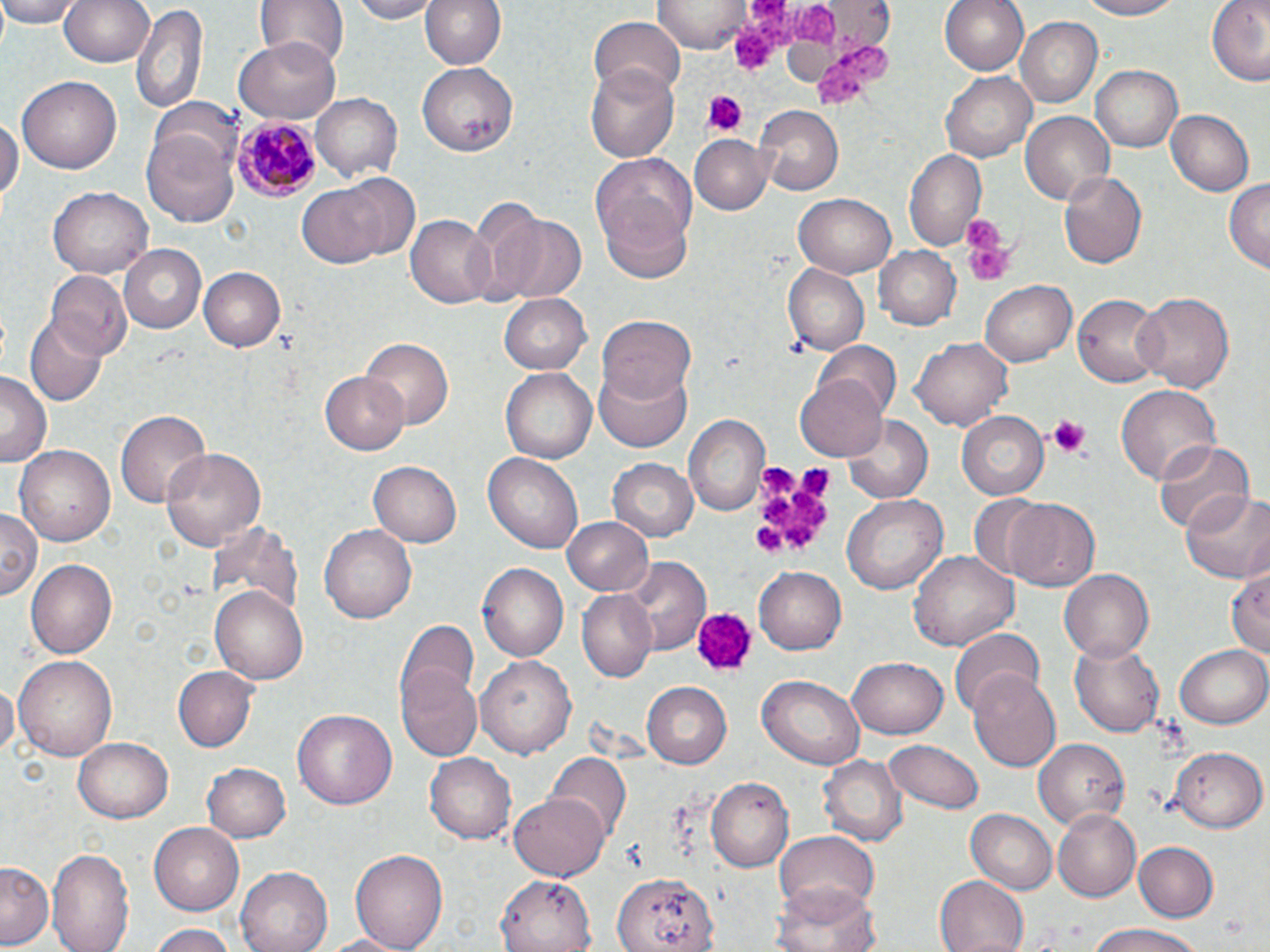

Summary:
  - Coordinate format: approximate bounding boxes as (x1, y1, x2, y2) in pixels
  - Uninfected red blood cell locations: (0, 0, 84, 27), (59, 0, 151, 68), (258, 0, 346, 68), (346, 0, 439, 22), (418, 0, 510, 70), (940, 0, 1031, 77), (1078, 0, 1189, 21), (1208, 0, 1270, 85), (652, 1, 755, 53), (131, 2, 208, 115), (590, 16, 686, 96), (1015, 17, 1101, 107), (234, 38, 342, 122), (417, 63, 519, 154), (1089, 65, 1183, 152), (585, 66, 679, 161), (941, 72, 1035, 162), (18, 76, 121, 174), (311, 94, 402, 181), (150, 98, 243, 175), (755, 107, 842, 196), (1166, 109, 1255, 196), (1021, 110, 1115, 204), (0, 113, 21, 205), (142, 130, 241, 228), (691, 133, 773, 212), (903, 147, 988, 254), (592, 152, 697, 271), (1058, 168, 1147, 271), (296, 174, 414, 270), (1224, 180, 1270, 273), (48, 187, 152, 279), (794, 194, 897, 277), (489, 212, 584, 301), (406, 215, 497, 307), (876, 245, 962, 331), (118, 246, 207, 333), (784, 260, 873, 354), (200, 266, 285, 352), (45, 271, 132, 360), (980, 279, 1077, 367), (1133, 291, 1232, 394), (498, 292, 591, 373), (1074, 292, 1165, 388), (27, 316, 106, 402), (597, 317, 695, 408), (358, 336, 454, 432), (913, 337, 1013, 430), (815, 339, 902, 420), (593, 363, 693, 452), (501, 370, 596, 464), (0, 372, 49, 465), (321, 372, 409, 455), (796, 373, 891, 462), (1115, 385, 1219, 486), (116, 407, 210, 507), (956, 411, 1049, 500), (686, 414, 769, 516), (842, 416, 933, 501), (1153, 438, 1254, 536), (14, 445, 115, 547), (159, 447, 266, 555), (483, 453, 584, 556), (609, 457, 697, 543), (369, 461, 461, 547), (1180, 489, 1270, 585), (965, 492, 1054, 583), (841, 493, 948, 594), (1007, 498, 1100, 592), (0, 505, 41, 600), (562, 516, 654, 596), (213, 521, 304, 619), (320, 524, 418, 624), (909, 550, 1018, 652), (627, 556, 710, 653), (25, 558, 118, 660), (478, 561, 570, 661), (753, 566, 848, 655), (1227, 568, 1270, 663), (1058, 569, 1153, 664), (211, 587, 309, 686), (577, 590, 657, 681), (396, 618, 482, 718), (947, 629, 1045, 719), (1069, 638, 1167, 737), (1175, 641, 1270, 729), (15, 654, 117, 762), (395, 655, 484, 764), (478, 655, 576, 758), (847, 656, 948, 739), (170, 664, 258, 752), (966, 670, 1063, 771), (759, 675, 862, 768), (0, 680, 18, 758), (643, 681, 732, 768), (291, 708, 397, 811), (74, 738, 173, 822), (1033, 738, 1128, 829), (883, 739, 984, 814), (1172, 747, 1264, 831), (424, 753, 515, 844), (548, 753, 630, 837), (821, 755, 907, 847), (202, 761, 291, 843), (706, 776, 794, 869), (512, 790, 609, 880), (1054, 808, 1142, 900), (965, 809, 1058, 893), (149, 822, 245, 916), (772, 829, 880, 912), (1135, 842, 1219, 921), (48, 845, 133, 952), (352, 846, 447, 952), (2, 862, 56, 948), (236, 865, 337, 952), (611, 869, 716, 952), (495, 872, 597, 951), (934, 874, 1025, 951), (773, 881, 882, 952), (147, 922, 239, 952), (1083, 923, 1206, 952), (319, 931, 412, 952)
  - Plasmodium malariae-infected red blood cell locations: (234, 116, 323, 199)
  - Platelet locations: (790, 3, 842, 48), (730, 24, 785, 71), (816, 43, 888, 110), (702, 90, 745, 137), (960, 215, 1016, 286), (1048, 414, 1091, 457), (746, 462, 833, 561), (699, 612, 755, 670)
  - Slide-level diagnosis: Plasmodium malariae
  - Magnification: 1000x
  - Stain: May-Grünwald-Giemsa
  - Preparation: thin blood film
  - Image size: 1270×952 pixels
  - Field of view: single
  - Modality: optical microscopy